Comment on the morphology of the erythrocytes.
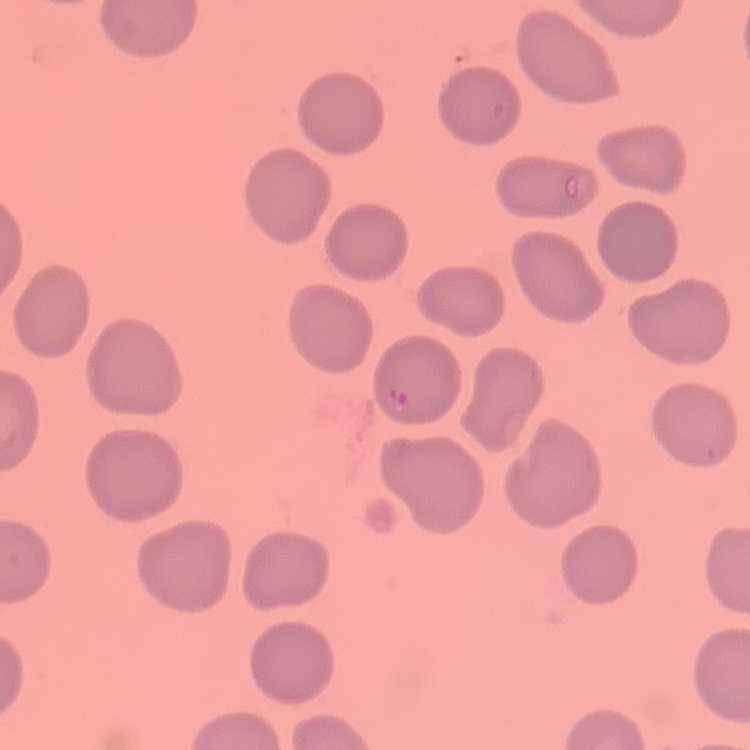

They show no rouleaux formation.

stain = Field's or Giemsa
image type = one tile cut from a larger photomicrograph
preparation = thin blood film